Comment on the morphology of the red blood cells.
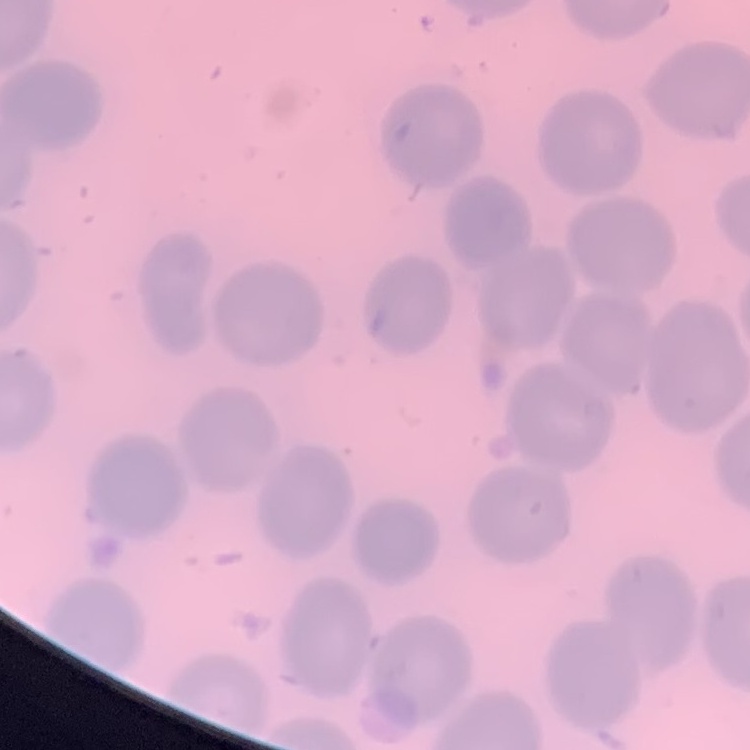

They show no rouleaux formation.

Square crop of a larger photomicrograph. Stained with either Field's or Giemsa. Thin blood smear.